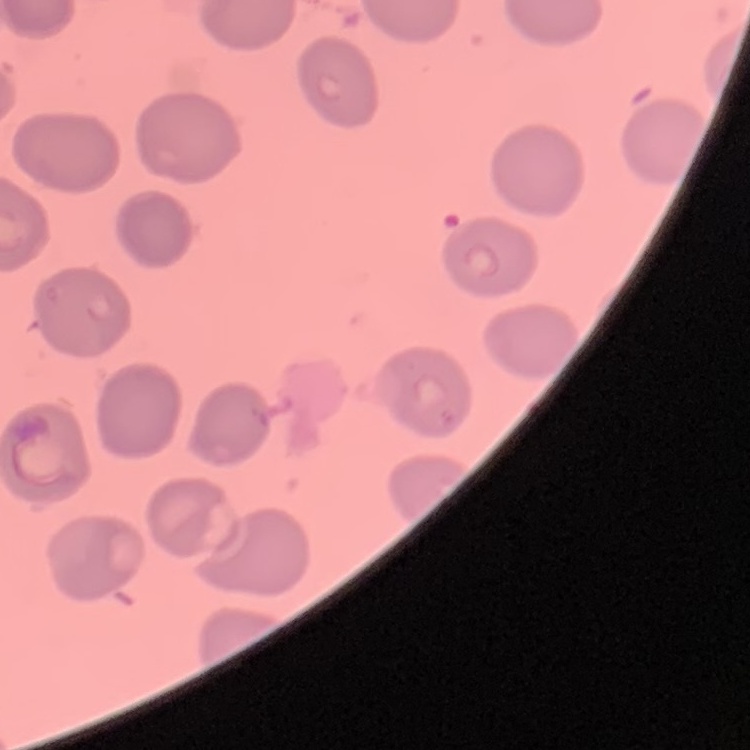
red blood cell morphology = no rouleaux formation
image type = one tile cut from a larger photomicrograph
stain = Field's or Giemsa
preparation = thin blood smear